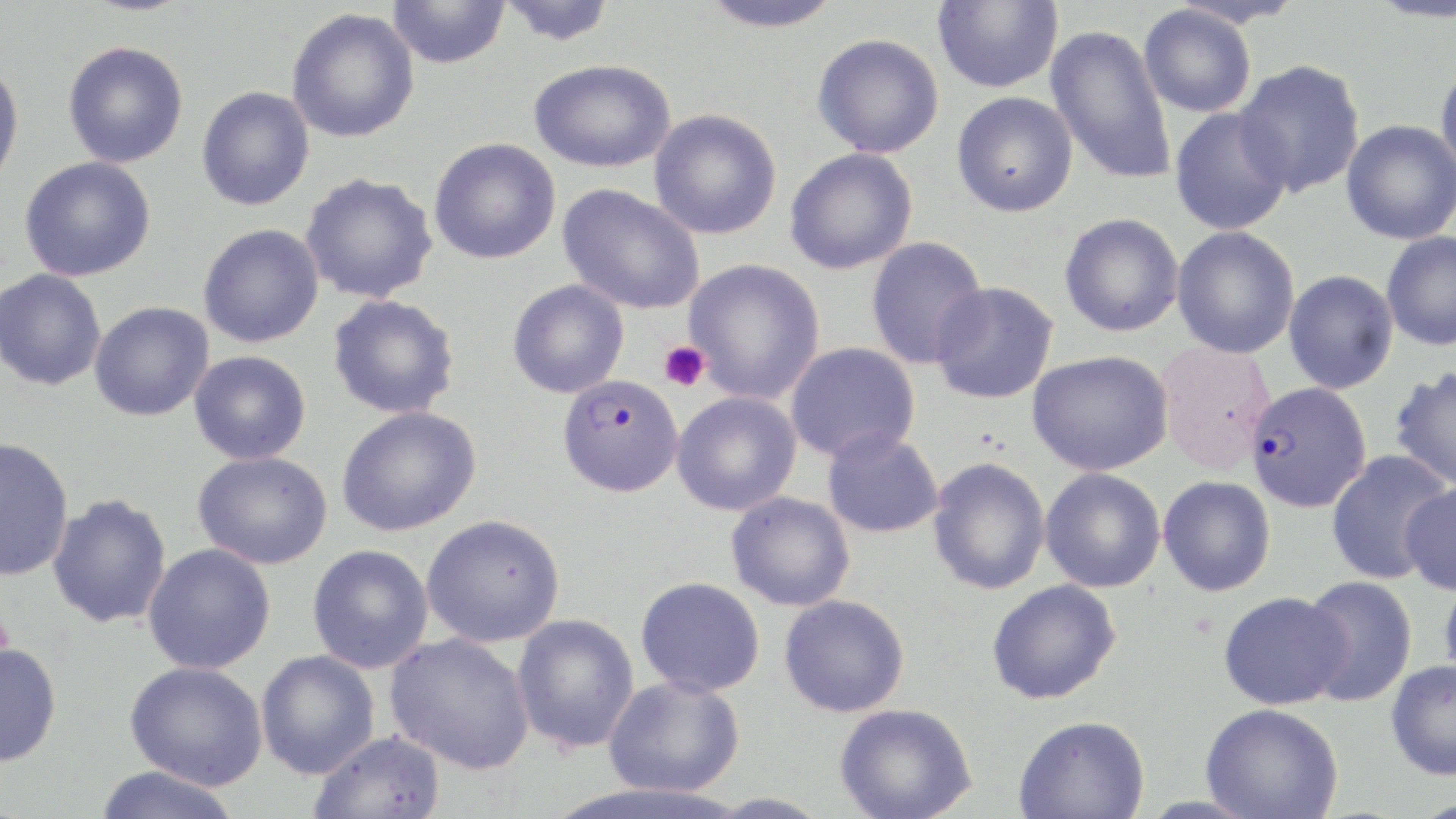

Summary:
  - Coordinate format: approximate bounding boxes as (x1, y1, x2, y2) in pixels
  - Plasmodium falciparum-infected red blood cell locations: (566, 381, 688, 499), (1244, 381, 1372, 514)
  - Platelet locations: (659, 341, 709, 392)
  - Uninfected red blood cell locations: (388, 0, 510, 68), (497, 0, 616, 46), (696, 0, 847, 33), (932, 0, 1063, 93), (1138, 5, 1257, 118), (287, 8, 420, 143), (1045, 25, 1178, 185), (812, 33, 944, 158), (62, 40, 188, 168), (1434, 56, 1456, 183), (529, 58, 676, 173), (0, 59, 25, 192), (1234, 59, 1366, 197), (197, 86, 314, 211), (951, 91, 1078, 218), (1169, 107, 1293, 236), (649, 108, 782, 240), (1341, 119, 1456, 245), (429, 138, 561, 264), (784, 147, 918, 275), (19, 156, 156, 282), (300, 172, 438, 303), (557, 184, 704, 315), (1059, 212, 1184, 337), (198, 223, 324, 348), (1172, 226, 1300, 359), (1381, 231, 1456, 351), (865, 236, 989, 369), (684, 258, 825, 404), (0, 269, 106, 391), (1283, 270, 1399, 394), (507, 279, 629, 398), (930, 281, 1060, 405), (328, 294, 460, 419), (89, 301, 214, 421), (785, 341, 920, 463), (189, 350, 311, 465), (1027, 350, 1174, 476), (1389, 366, 1456, 490), (671, 391, 802, 516), (336, 406, 481, 536), (822, 428, 944, 538), (0, 437, 74, 582), (1325, 450, 1452, 585), (192, 451, 332, 570), (928, 457, 1051, 595), (1040, 467, 1166, 593), (1158, 475, 1276, 596), (1399, 482, 1456, 595), (726, 491, 855, 612), (47, 493, 172, 629), (421, 514, 565, 647), (142, 543, 276, 675), (307, 544, 434, 674), (1439, 572, 1456, 689), (1300, 575, 1418, 706), (636, 576, 765, 697), (986, 578, 1121, 704), (1218, 591, 1351, 710), (779, 594, 910, 717), (511, 613, 640, 754), (385, 633, 535, 775), (0, 642, 62, 768), (255, 650, 380, 779), (1385, 659, 1456, 780), (124, 661, 268, 789), (603, 676, 745, 797), (1201, 703, 1343, 819), (834, 704, 977, 819), (1013, 714, 1150, 818), (309, 730, 446, 819), (92, 765, 244, 819), (704, 792, 835, 817)
  - Slide-level diagnosis: Plasmodium falciparum
  - Preparation: thin blood film
  - Modality: light microscopy
  - Magnification: 1000x
  - Field of view: one of a larger specimen
  - Image size: 1456×819 pixels
  - Stain: May-Grünwald-Giemsa